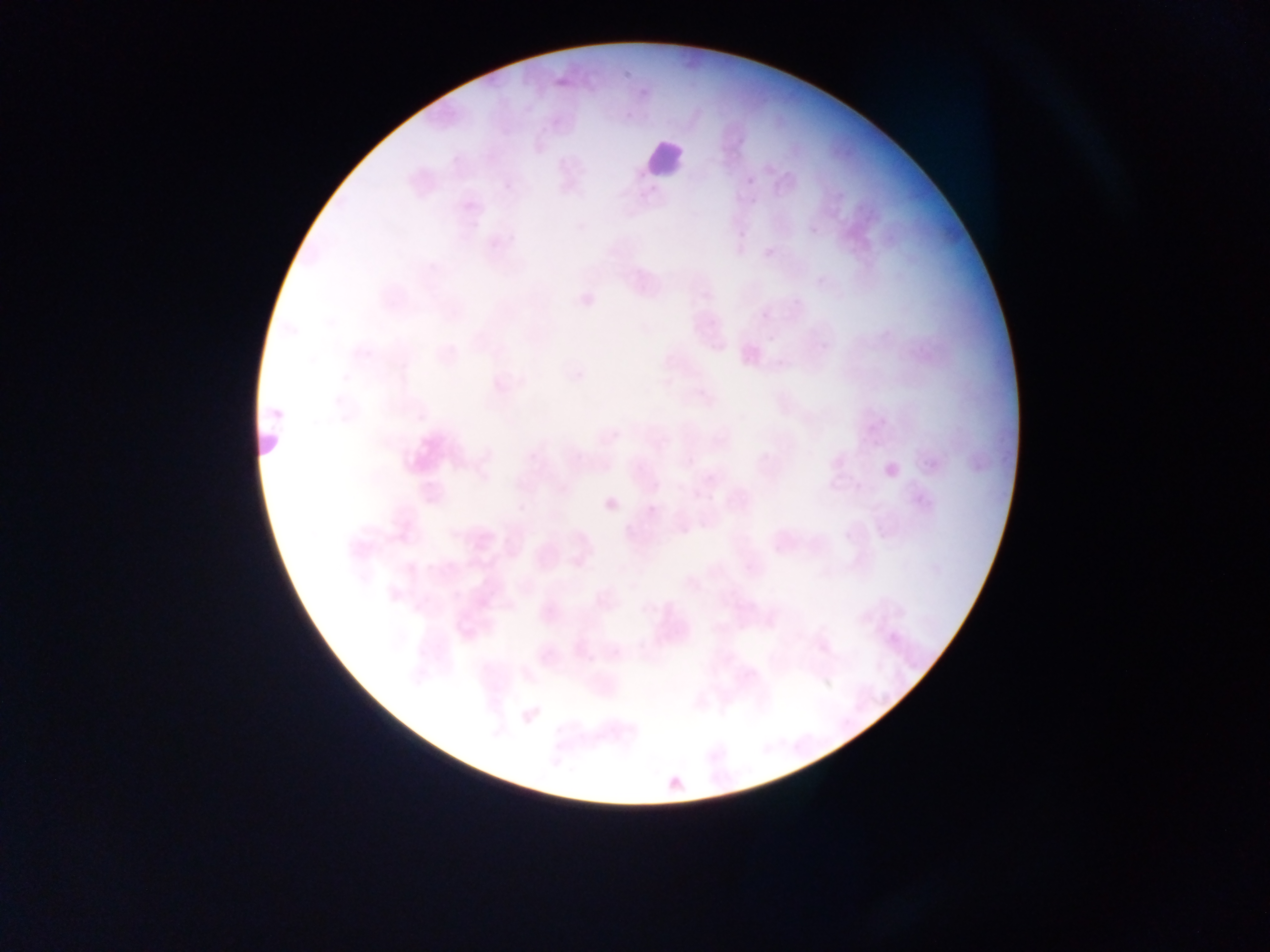
Approximate bounding boxes as left top right bottom in pixels. Leukocyte locations: 638 141 684 177. Malaria parasite locations: 808 225 819 236; 879 416 888 427; 855 482 864 491; 692 490 701 499; 647 505 657 515; 609 646 621 658. Thin blood film. One field of view. Photographed through a microscope with a mobile-phone camera. Image is 1270×952 pixels. Collected in Ghana.